State the preparation type.
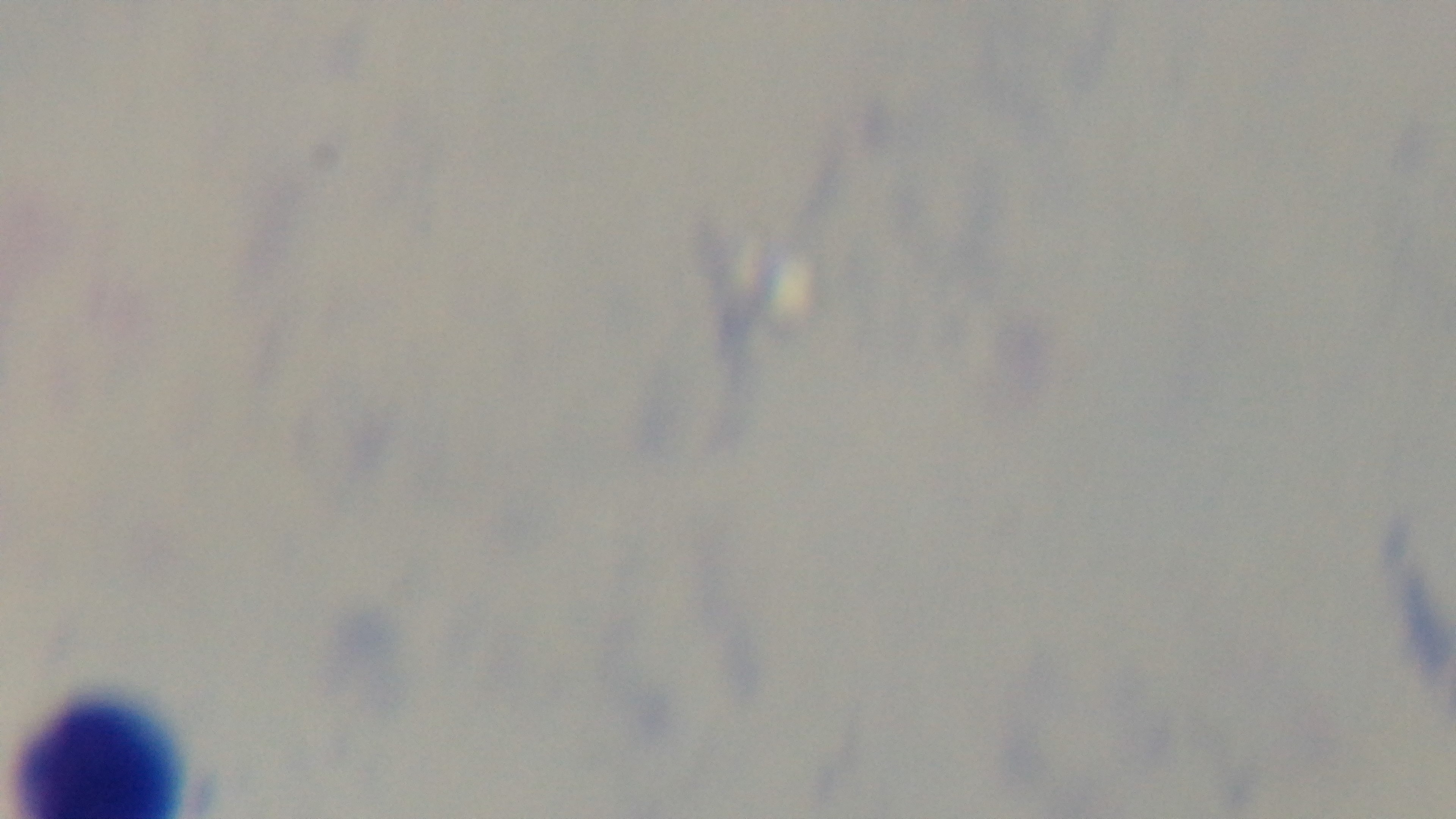

A thick smear.

objective = 100x oil immersion
capture = mounted 4K digital camera
stain = Giemsa
malaria status = uninfected
modality = light microscopy
field of view = one from the slide